Classify this cell by malaria status.
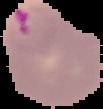
Parasitized.

image type = segmented cell region with the area outside set to black
preparation = thin blood film
image size = 103×109 pixels